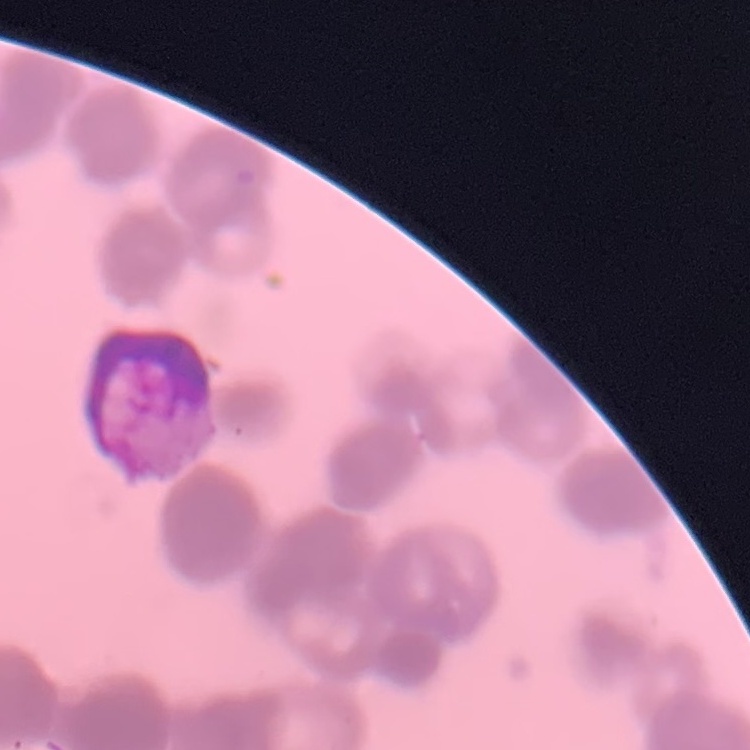

Summary:
  - Red blood cell morphology: rouleaux formation
  - Stain: Field's or Giemsa
  - Image type: square crop of a larger photomicrograph
  - Preparation: thin blood film